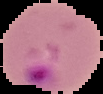

image size = 103×94 pixels
image type = segmented cell region on a black background
result = malaria parasites detected
preparation = thin blood film